Assess the morphology of the red blood cells.
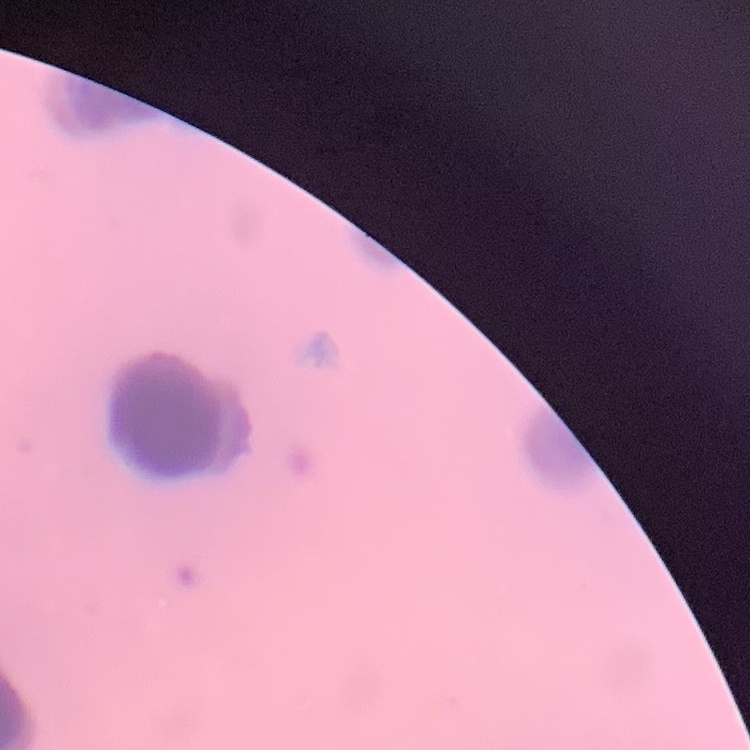

They show rouleaux formation.

{
  "image_type": "square crop of a larger photomicrograph",
  "preparation": "thin blood smear",
  "stain": "Field's or Giemsa"
}